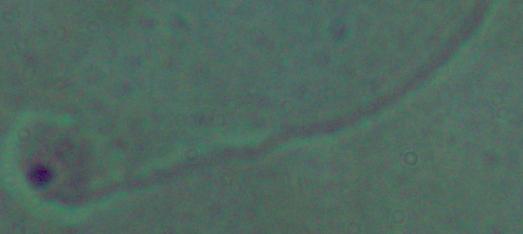

Summary:
  - Modality: micrograph
  - Magnification: 1000x
  - Identification: Leishmania